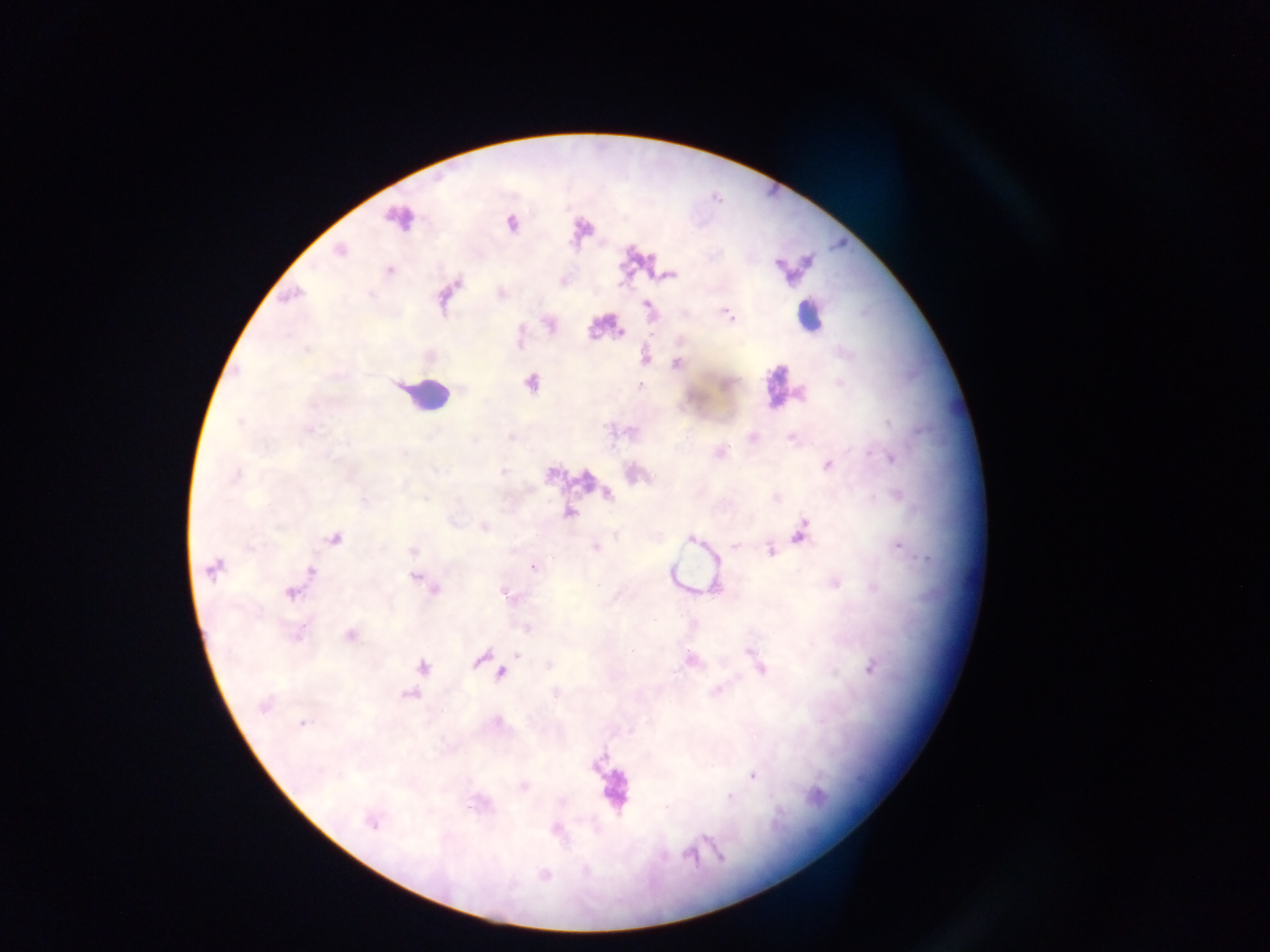

capture = mobile-phone photograph through a microscope
Plasmodium parasite locations = approximate centers as [x, y] in pixels: [511, 224], [341, 251], [389, 271], [668, 275], [501, 293], [292, 295], [648, 306], [728, 314], [550, 325], [621, 332], [307, 349], [645, 358], [678, 364], [531, 383], [641, 386], [240, 422], [889, 423], [309, 430], [752, 438], [791, 438], [872, 455], [892, 458], [827, 465], [503, 473], [234, 475], [608, 494], [425, 499], [570, 513], [484, 527], [800, 532], [334, 538], [691, 540], [734, 546], [595, 547], [899, 547], [771, 550], [413, 551], [533, 567], [212, 570], [311, 571], [416, 577], [835, 583], [434, 589], [290, 594], [507, 596], [527, 628], [350, 635], [517, 655], [481, 658], [690, 660], [760, 667], [423, 668], [871, 668], [501, 674], [717, 691], [556, 694], [411, 695], [264, 705], [302, 723], [753, 777], [524, 786], [730, 797], [372, 823], [557, 830], [689, 855], [720, 856], [544, 875]
leukocyte locations = approximate centers as [x, y] in pixels: [398, 222], [808, 314], [781, 383], [427, 395], [612, 789]
country = Ghana
image size = 1270×952 pixels
field of view = single
preparation = thick blood smear